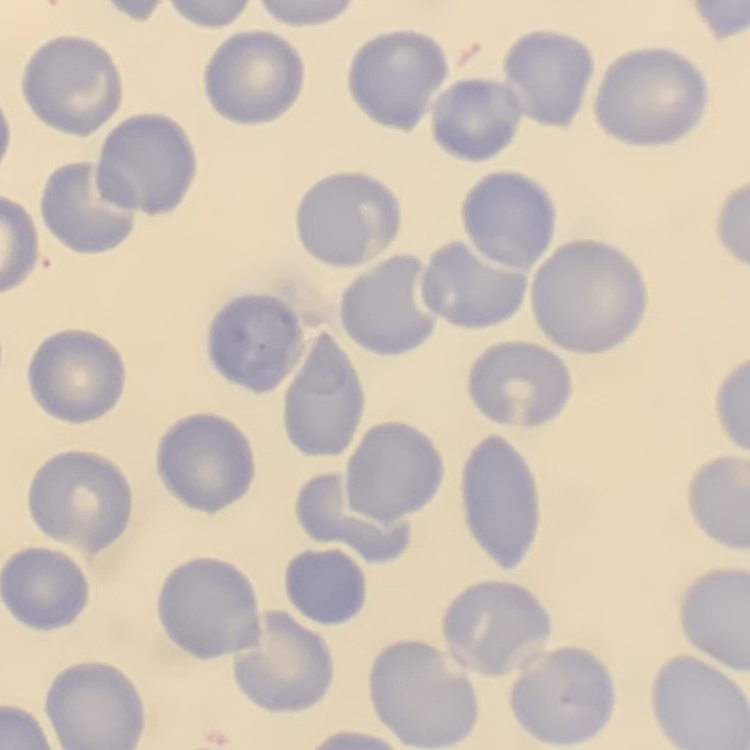 The red blood cells show no rouleaux formation. Square crop of a larger photomicrograph. Thin blood film. Field's or Giemsa stain.